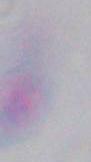

Captured at 1000x magnification. Micrograph. Toxoplasma gondii is seen.